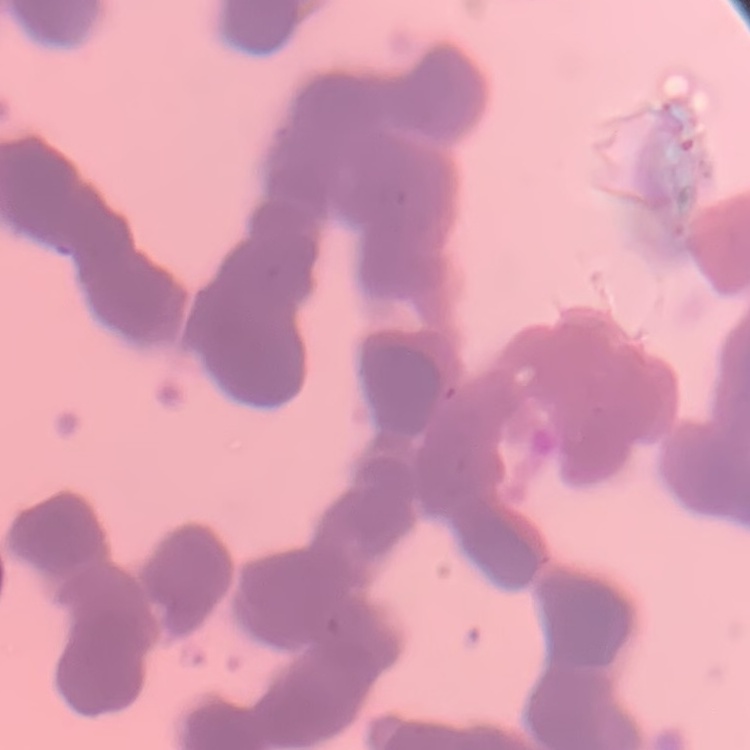
erythrocyte morphology = rouleaux formation
preparation = thin peripheral smear
image type = one tile cut from a larger photomicrograph
stain = Field's or Giemsa